Classify this cell by malaria status.
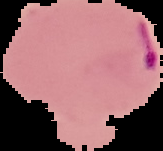
It is parasitized.

image_type: cell region segmented out of the field of view; surrounding area masked to black
preparation: thin blood smear
image_size: 163×151 pixels